Classify the preparation.
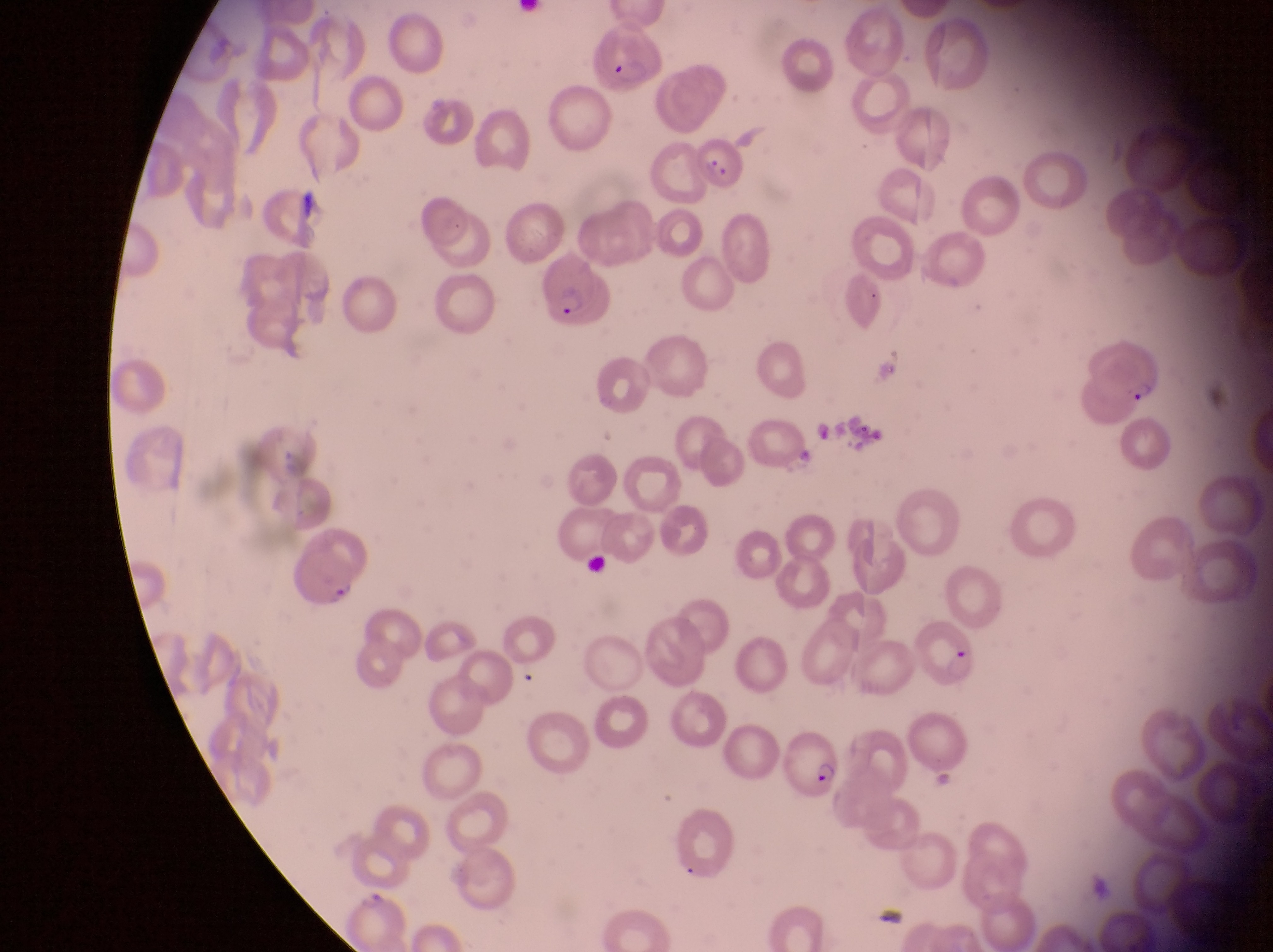
Thin blood smear.

country = Uganda
parasitised red blood cell locations = approximate bounding boxes as {left, top, right, bottom} in pixels: {585, 28, 661, 95}, {691, 134, 746, 194}, {541, 267, 616, 329}, {1078, 322, 1161, 409}, {285, 545, 363, 610}, {916, 614, 981, 691}, {781, 731, 843, 803}
capture = smartphone photograph through the eyepiece of an Olympus CX-23 microscope
image size = 1273×952 pixels
magnification = 1000x
field of view = single